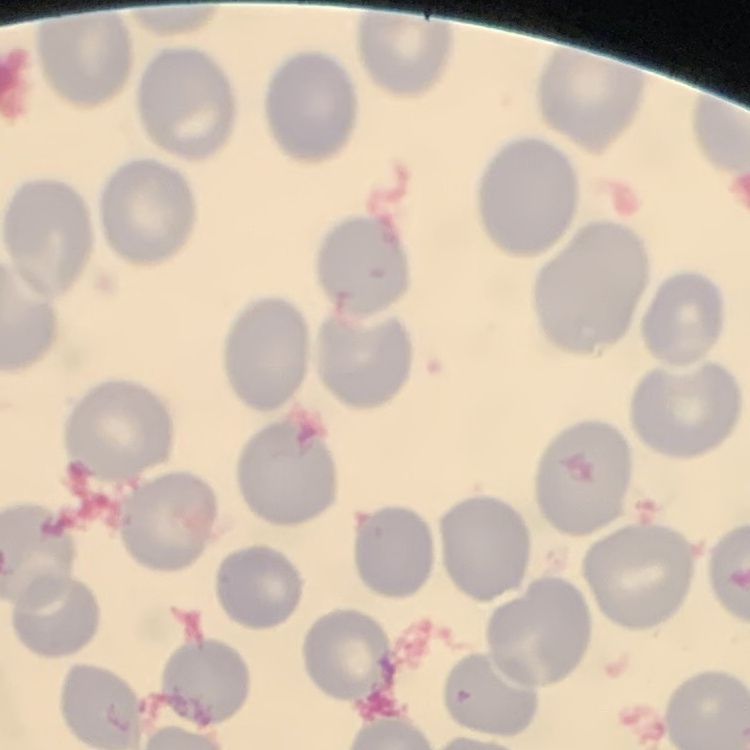

{
  "red_blood_cell_morphology": "no rouleaux formation",
  "image_type": "square crop of a larger photomicrograph",
  "preparation": "thin blood smear",
  "stain": "Field's or Giemsa"
}